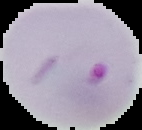

image type = segmented cell region on a black background
preparation = thin blood film
malaria status = parasitized
image size = 142×130 pixels